State the preparation type.
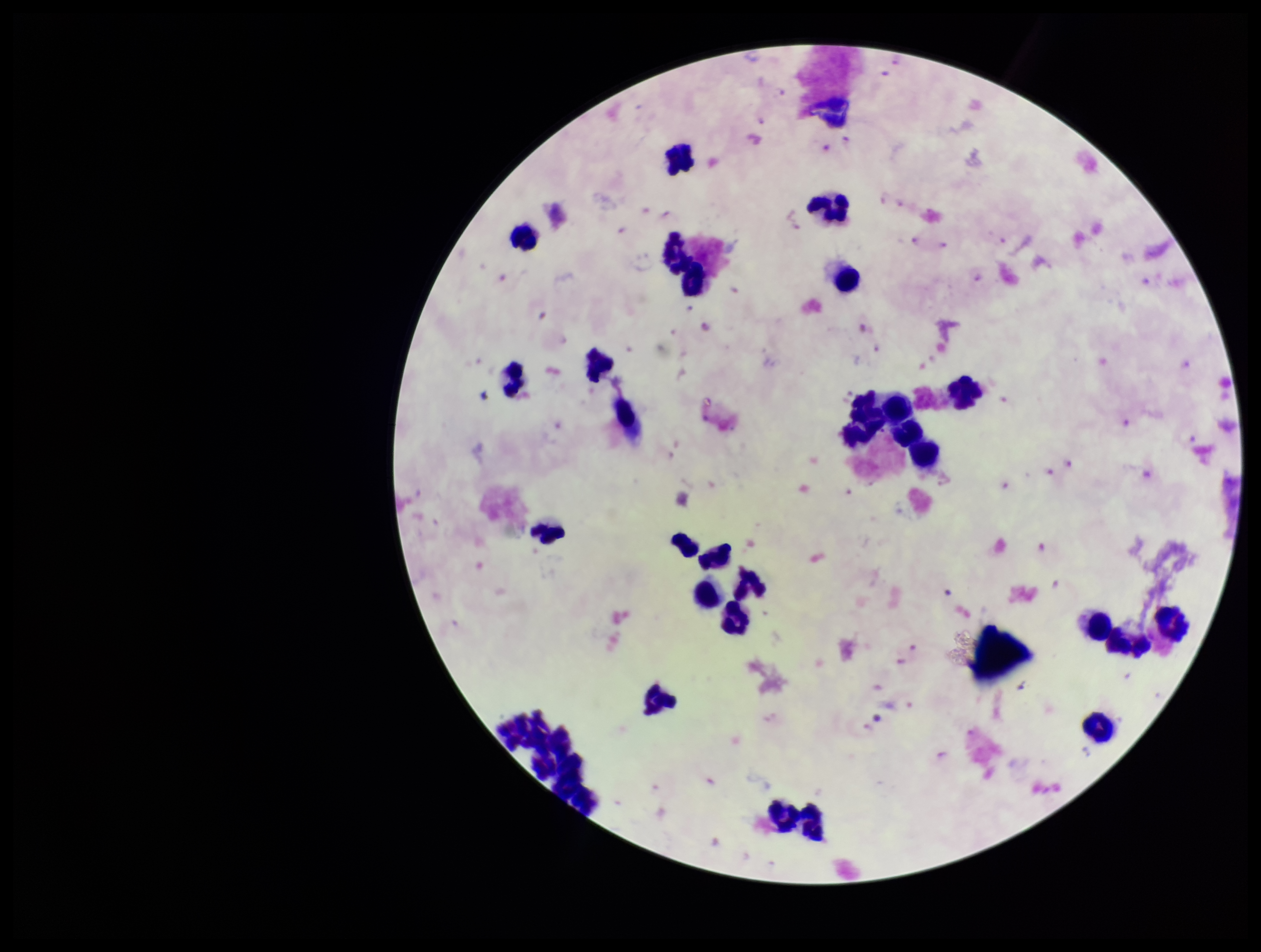

A thick smear.

Parasite count: 37. Stained with Giemsa. Leukocyte count: 27. Species reported for this patient: Plasmodium falciparum. Image is 1261×952 pixels. Patient malaria status: infected. Smartphone photograph taken through the eyepiece of a microscope. Single field of view. Plasmodium parasites: seen.